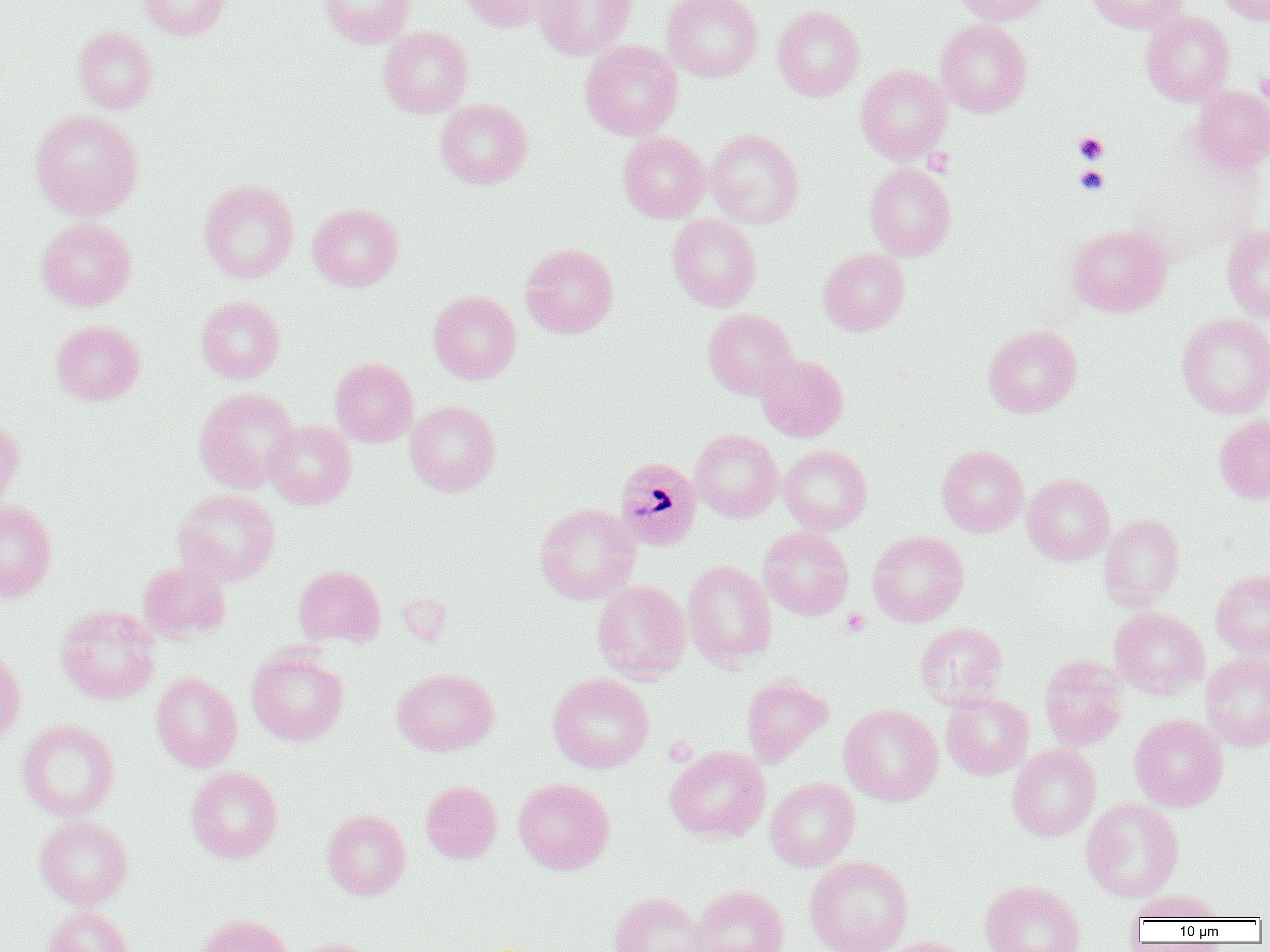
slide-level diagnosis = Plasmodium malariae
magnification = 1000x
Plasmodium malariae-infected red blood cell locations = approximate bounding boxes as [x1, y1, x2, y2] in pixels: [614, 456, 702, 551]
preparation = thin blood smear
modality = light microscopy
image size = 1270×952 pixels
uninfected red blood cell locations = approximate bounding boxes as [x1, y1, x2, y2] in pixels: [138, 0, 231, 40], [318, 0, 416, 47], [458, 0, 550, 33], [534, 0, 637, 60], [662, 0, 762, 82], [953, 0, 1054, 25], [1084, 0, 1188, 32], [1214, 0, 1270, 25], [772, 4, 865, 102], [1141, 10, 1235, 106], [936, 19, 1032, 117], [73, 26, 157, 114], [378, 26, 473, 118], [580, 40, 683, 140], [856, 65, 951, 163], [1189, 85, 1270, 173], [436, 99, 532, 189], [30, 110, 144, 219], [705, 128, 804, 227], [618, 132, 709, 223], [865, 163, 956, 261], [198, 180, 299, 283], [308, 203, 403, 291], [667, 215, 761, 311], [37, 218, 137, 310], [1222, 224, 1270, 322], [1067, 225, 1171, 317], [521, 243, 618, 339], [818, 248, 910, 336], [429, 291, 522, 384], [196, 296, 285, 383], [703, 308, 798, 399], [1176, 312, 1270, 418], [51, 320, 145, 406], [983, 325, 1083, 417], [755, 353, 849, 441], [330, 357, 418, 447], [194, 388, 300, 493], [405, 401, 501, 496], [1214, 414, 1270, 504], [0, 419, 24, 513], [264, 420, 356, 509], [691, 429, 782, 522], [779, 445, 872, 534], [937, 445, 1028, 536], [1022, 473, 1114, 566], [174, 489, 280, 585], [0, 501, 57, 601], [534, 503, 640, 604], [1099, 514, 1184, 610], [758, 526, 854, 620], [867, 530, 969, 626], [682, 560, 776, 669], [137, 561, 230, 643], [294, 564, 385, 647], [1210, 568, 1270, 660], [592, 580, 691, 683], [56, 605, 160, 704], [1109, 607, 1209, 698], [915, 622, 1008, 710], [247, 647, 348, 746], [0, 648, 26, 748], [1201, 653, 1270, 750], [1039, 656, 1128, 751], [392, 668, 499, 756], [547, 672, 654, 773], [152, 673, 242, 772], [741, 674, 833, 766], [941, 692, 1034, 779], [838, 703, 943, 806], [1129, 713, 1228, 811], [17, 719, 120, 820], [1008, 744, 1100, 841], [665, 745, 771, 842], [185, 766, 283, 863], [513, 777, 615, 874], [765, 777, 860, 871], [420, 781, 502, 864], [1081, 797, 1184, 901], [322, 808, 411, 900], [35, 816, 133, 908], [804, 855, 913, 952], [979, 879, 1085, 952], [689, 884, 789, 952], [1128, 889, 1225, 923], [608, 892, 708, 952], [43, 906, 132, 952], [195, 914, 293, 952], [876, 936, 974, 952], [287, 938, 380, 952]
field of view = one of a larger specimen
platelet locations = approximate bounding boxes as [x1, y1, x2, y2] in pixels: [1255, 71, 1270, 105], [1074, 132, 1108, 164], [922, 148, 954, 177], [1075, 165, 1110, 196], [841, 609, 870, 636]